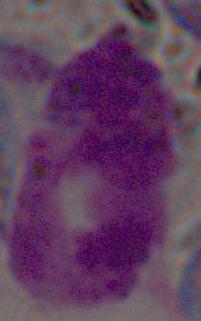 Micrograph. A white blood cell is shown. 1000x magnification.